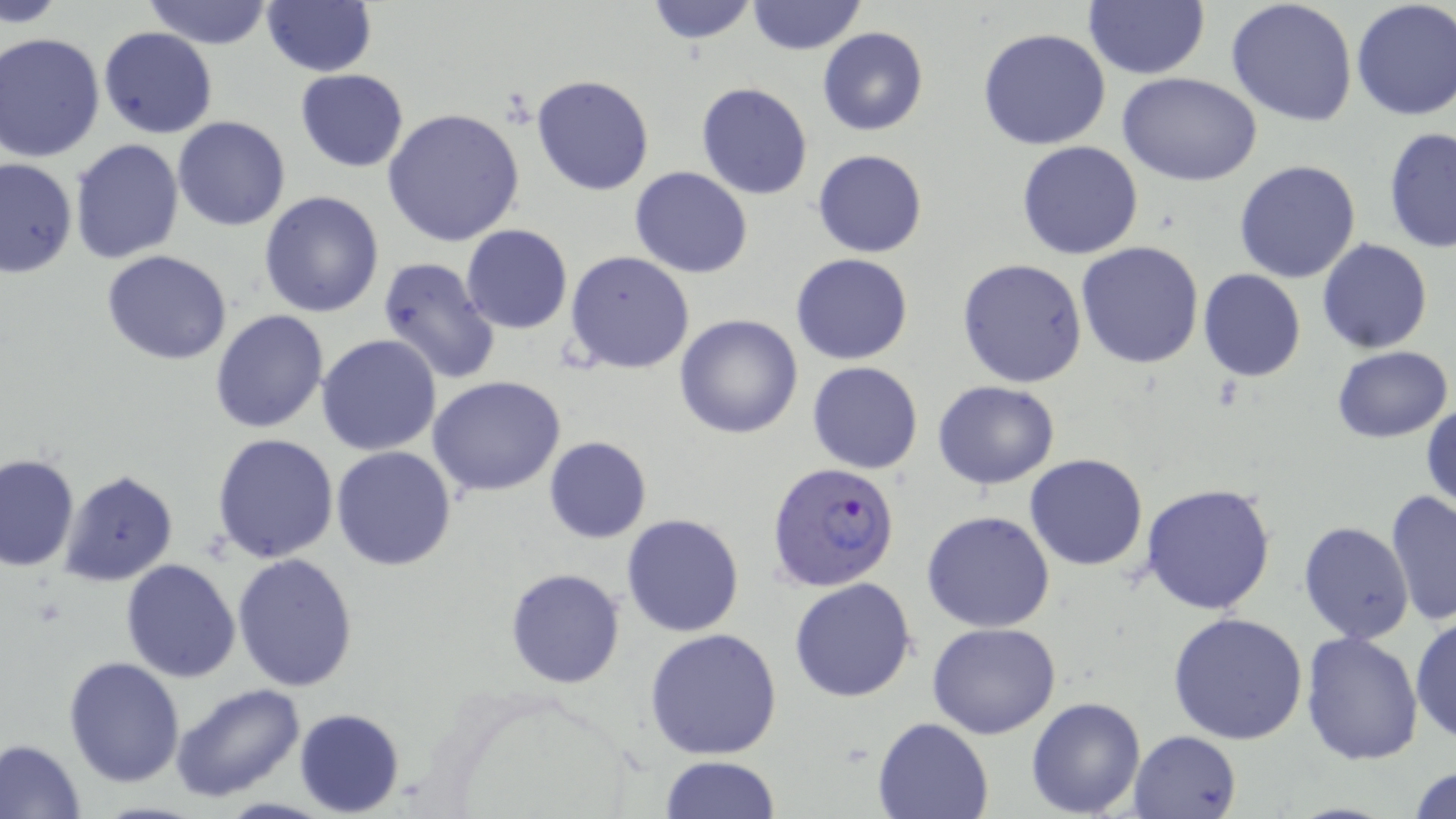
{
  "slide_level_diagnosis": "Plasmodium falciparum",
  "uninfected_red_blood_cell_locations": "approximate bounding boxes as [x1, y1, x2, y2] in pixels: [1, 0, 67, 28], [141, 0, 275, 49], [641, 0, 762, 46], [747, 0, 866, 55], [1227, 0, 1358, 128], [1351, 0, 1456, 121], [261, 2, 377, 75], [1083, 2, 1209, 80], [97, 26, 218, 138], [978, 27, 1110, 150], [818, 28, 928, 134], [0, 32, 105, 162], [295, 69, 409, 171], [1119, 73, 1261, 186], [532, 74, 654, 194], [695, 82, 813, 200], [384, 107, 525, 248], [172, 116, 291, 231], [1382, 129, 1455, 254], [68, 139, 185, 264], [1016, 141, 1145, 259], [812, 149, 928, 258], [0, 157, 76, 278], [1233, 158, 1362, 283], [629, 167, 754, 278], [259, 191, 385, 318], [460, 225, 573, 334], [1317, 237, 1432, 355], [1076, 241, 1205, 369], [102, 250, 232, 364], [564, 250, 694, 375], [792, 253, 912, 364], [376, 256, 501, 386], [958, 258, 1089, 389], [1198, 269, 1306, 382], [210, 311, 329, 433], [674, 314, 804, 439], [316, 334, 443, 457], [1333, 346, 1453, 442], [807, 361, 924, 474], [427, 375, 566, 498], [933, 379, 1059, 489], [1421, 400, 1455, 518], [212, 433, 339, 563], [543, 436, 652, 543], [330, 447, 457, 570], [0, 452, 79, 573], [1025, 452, 1148, 571], [59, 469, 179, 588], [1140, 482, 1278, 614], [1385, 489, 1455, 628], [922, 511, 1055, 631], [622, 514, 745, 637], [1299, 522, 1414, 644], [232, 553, 360, 691], [120, 558, 241, 683], [504, 567, 625, 689], [789, 577, 917, 702], [1167, 611, 1311, 745], [1410, 612, 1456, 745], [927, 622, 1060, 738], [645, 627, 785, 760], [1299, 630, 1425, 764], [63, 657, 186, 788], [172, 682, 306, 803], [1026, 697, 1146, 816], [294, 709, 405, 817], [872, 715, 995, 819], [1128, 729, 1241, 818], [0, 738, 87, 817], [659, 755, 782, 818], [1407, 762, 1456, 819]",
  "field_of_view": "single",
  "plasmodium_falciparum_infected_red_blood_cell_locations": "approximate bounding boxes as [x1, y1, x2, y2] in pixels: [765, 462, 901, 594]",
  "preparation": "thin blood smear",
  "modality": "light microscopy",
  "magnification": "1000x",
  "stain": "May-Grünwald-Giemsa",
  "image_size": "1456×819 pixels"
}